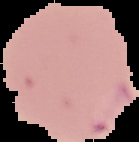

{
  "image_size": "139×142 pixels",
  "malaria_status": "parasitized",
  "image_type": "cell region segmented out of the field of view; surrounding area masked to black",
  "preparation": "thin blood film"
}